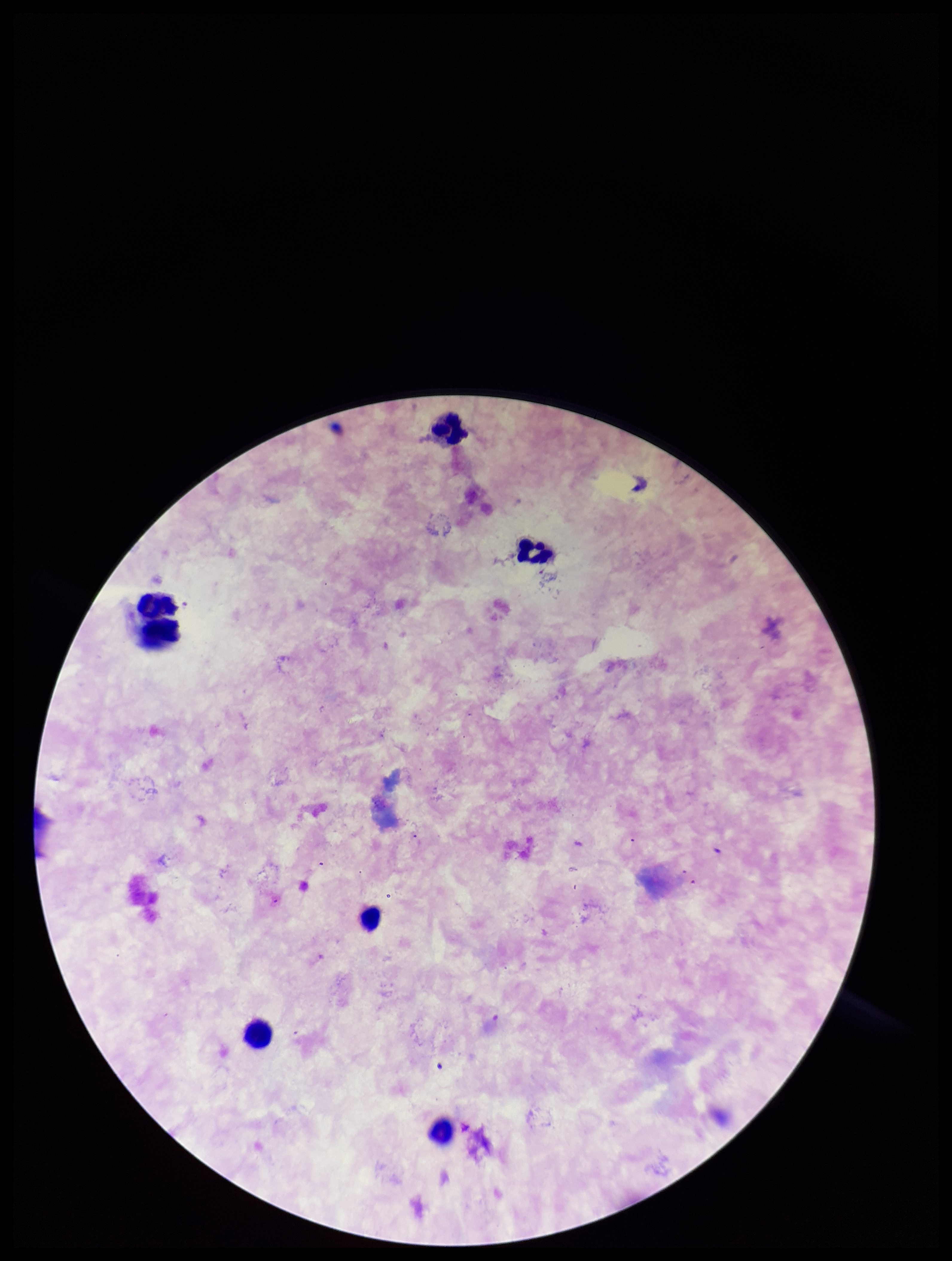

stain = Giemsa
parasite count = 0
preparation = thick
leukocyte count = 6
patient malaria status = negative
field of view = single
Plasmodium parasites = none identified
capture = smartphone photograph through the microscope eyepiece
image size = 952×1261 pixels